Point out each leukocyte.
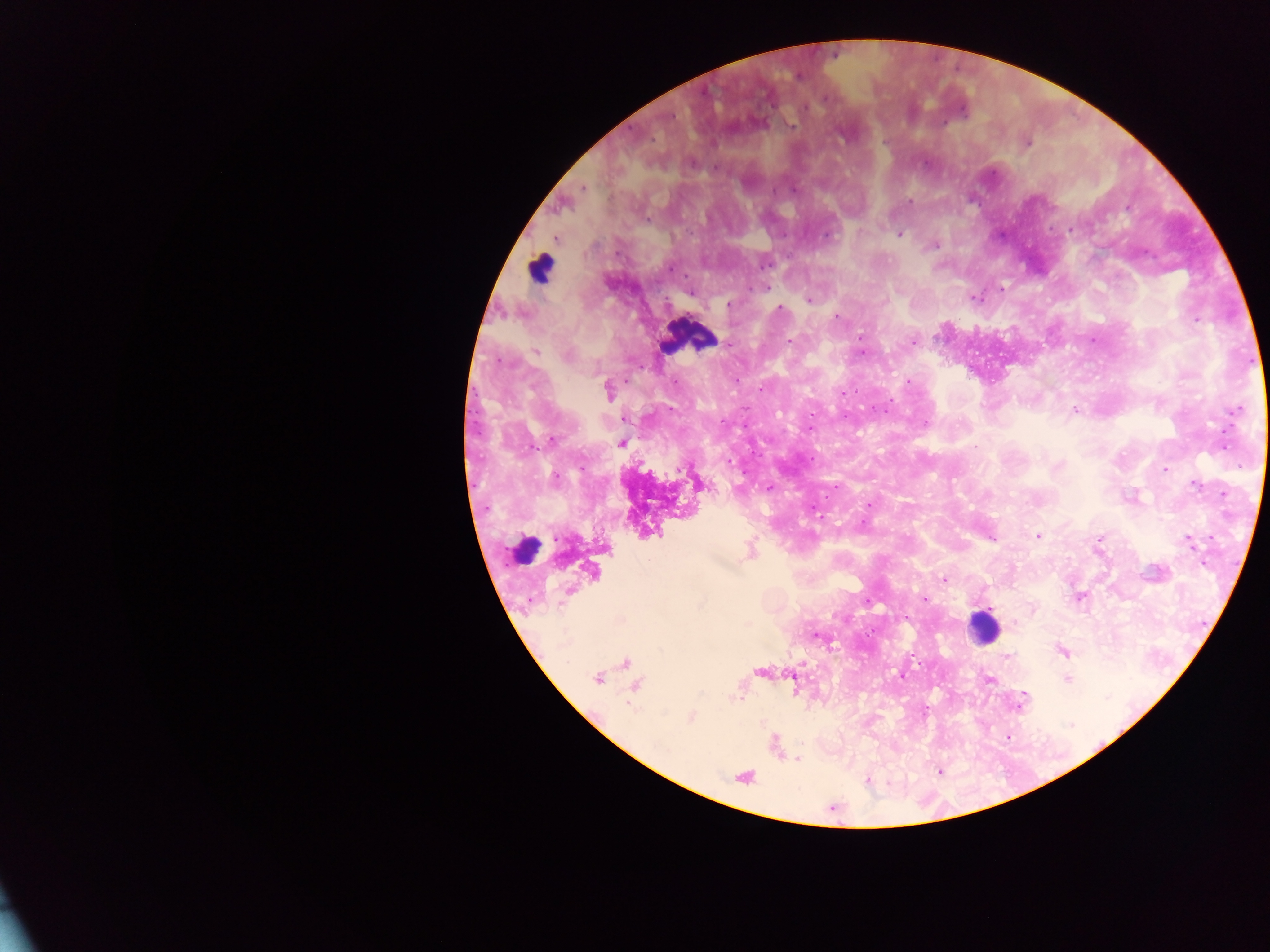
Approximate centers as x y in pixels.
Leukocytes: 540 267; 690 335; 524 551; 983 627.

Summary:
  - Malaria parasite locations: 1026 142; 582 187; 908 202; 647 218; 900 234; 827 235; 935 245; 765 286; 1001 287; 973 297; 809 299; 728 304; 780 308; 836 316; 1195 320; 1092 339; 790 341; 913 341; 536 351; 908 382; 607 391; 842 393; 1075 409; 1236 409; 623 418; 551 439; 621 442; 1163 469; 1196 484; 767 486; 836 487; 1224 494; 869 503; 1037 535; 990 537; 1099 539; 1188 540; 1097 550; 750 551; 944 580; 922 597; 1080 597; 1063 651; 1005 657; 626 662; 761 671; 901 676; 598 677; 988 678; 1066 678; 634 685; 1022 698; 691 717; 1006 736; 796 758; 939 771; 743 777; 868 781
  - Capture: mobile-phone photograph through a microscope
  - Preparation: thick blood smear
  - Country: Ghana
  - Field of view: single
  - Image size: 1270×952 pixels